Locate and identify every blood parasite.
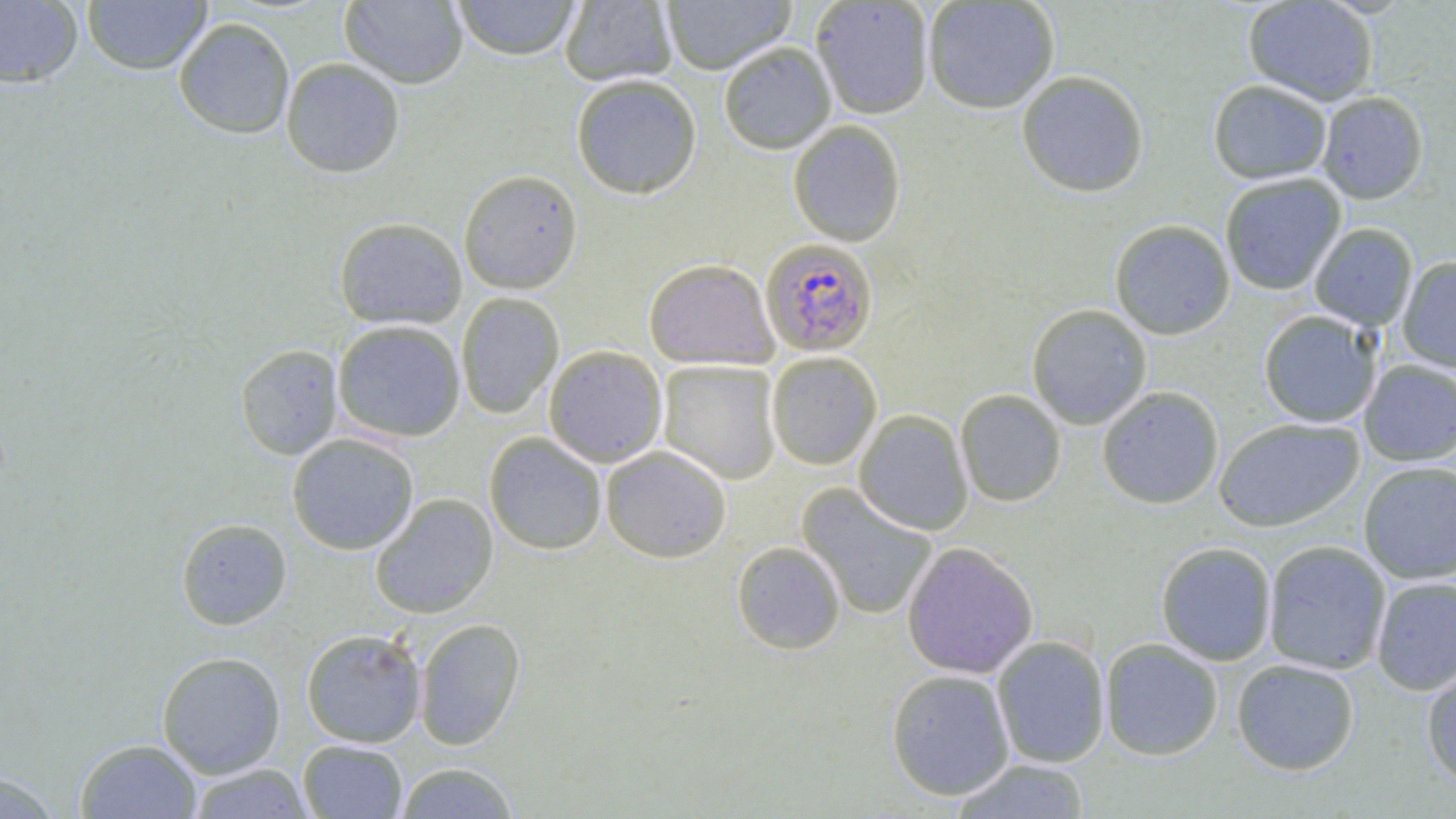
Approximate bounding boxes as [x1, y1, x2, y2] in pixels.
Plasmodium falciparum-infected red blood cells: [760, 240, 877, 357].
No Plasmodium ovale, Plasmodium malariae, Plasmodium vivax, Babesia divergens, or Trypanosoma brucei observed.

Summary:
  - Uninfected red blood cell locations: [340, 0, 468, 89], [451, 0, 582, 63], [560, 0, 677, 88], [661, 0, 797, 75], [922, 0, 1060, 116], [1243, 0, 1378, 107], [0, 1, 83, 88], [82, 1, 212, 74], [811, 1, 933, 120], [173, 18, 295, 139], [718, 44, 837, 156], [280, 58, 405, 178], [1016, 73, 1149, 199], [571, 77, 702, 201], [1208, 82, 1332, 186], [1317, 94, 1429, 206], [788, 122, 906, 248], [458, 171, 583, 295], [1220, 175, 1346, 296], [334, 217, 467, 330], [1109, 222, 1235, 341], [1309, 224, 1417, 331], [1396, 257, 1456, 372], [643, 260, 779, 372], [456, 293, 564, 420], [1026, 305, 1152, 430], [1258, 311, 1381, 429], [332, 320, 466, 442], [235, 344, 343, 460], [543, 346, 667, 468], [766, 352, 882, 470], [658, 360, 781, 485], [1359, 360, 1456, 466], [1097, 388, 1224, 510], [955, 390, 1067, 508], [854, 410, 973, 536], [1214, 419, 1364, 533], [286, 433, 420, 555], [484, 433, 607, 555], [601, 446, 731, 563], [1358, 462, 1456, 584], [797, 485, 938, 620], [370, 493, 498, 619], [176, 518, 292, 630], [731, 541, 845, 655], [1263, 541, 1391, 675], [901, 542, 1039, 680], [1155, 542, 1277, 666], [1371, 576, 1456, 695], [414, 618, 526, 750], [301, 628, 427, 748], [992, 637, 1110, 768], [1100, 639, 1223, 761], [157, 651, 286, 778], [1231, 659, 1360, 776], [1421, 661, 1456, 788], [887, 670, 1014, 800], [75, 739, 203, 819], [298, 740, 407, 818], [949, 759, 1090, 818], [394, 762, 520, 818], [186, 763, 315, 818], [0, 771, 62, 818]
  - Slide-level diagnosis: Plasmodium falciparum
  - Magnification: 1000x
  - Field of view: single
  - Stain: May-Grünwald-Giemsa
  - Image size: 1456×819 pixels
  - Preparation: thin blood film
  - Modality: light microscopy